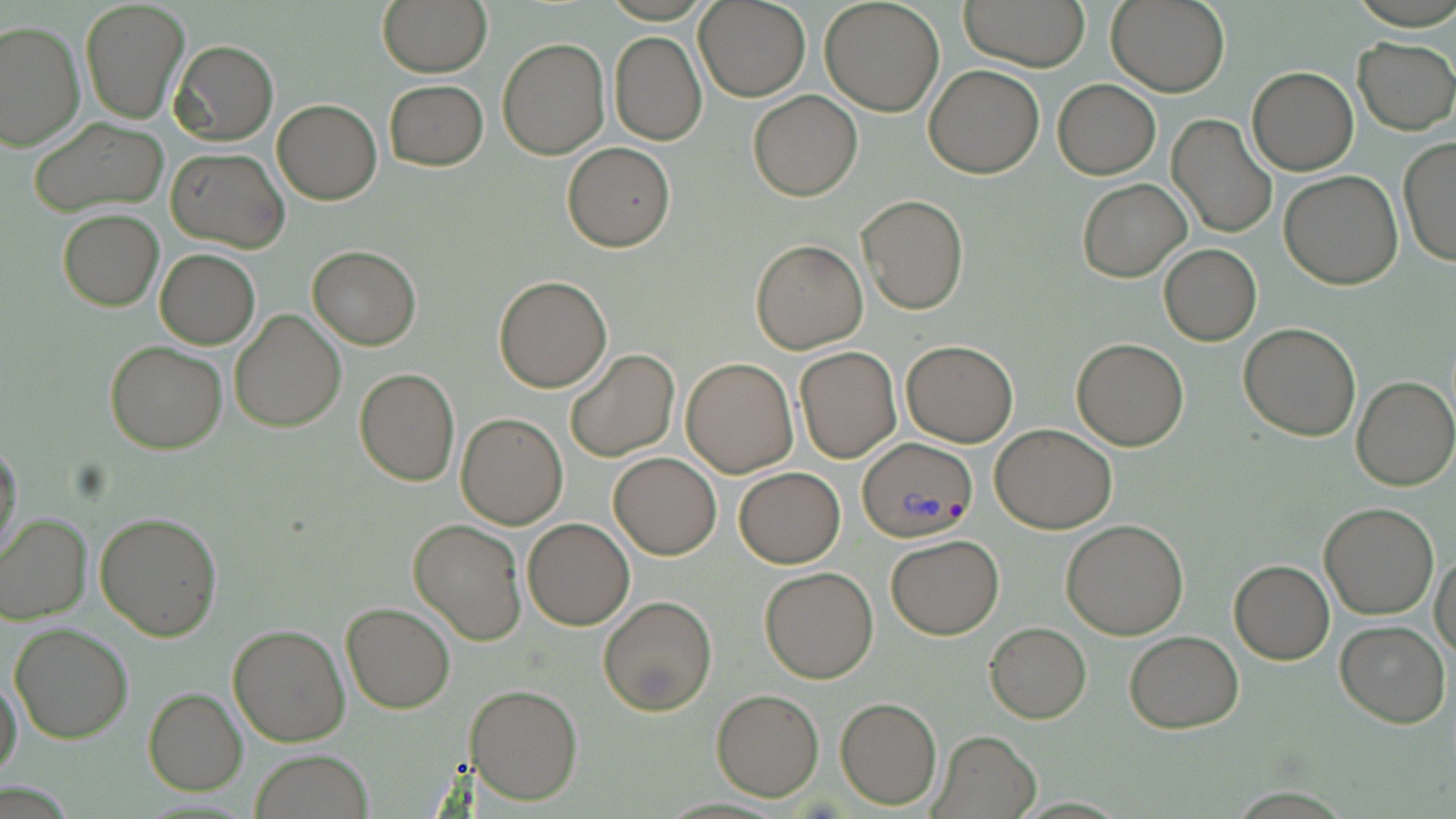
Approximate bounding boxes as [x1, y1, x2, y2] in pixels. Plasmodium vivax-infected red blood cell locations: [856, 437, 974, 543]. Uninfected red blood cell locations: [376, 0, 492, 77], [820, 0, 945, 117], [962, 0, 1091, 72], [1107, 0, 1230, 97], [80, 1, 189, 124], [694, 1, 810, 102], [0, 21, 85, 152], [609, 31, 707, 145], [497, 37, 610, 158], [1352, 37, 1456, 133], [170, 39, 278, 147], [924, 63, 1044, 179], [1247, 67, 1359, 176], [1053, 78, 1159, 179], [385, 79, 488, 170], [749, 90, 861, 202], [272, 98, 382, 205], [1167, 113, 1277, 239], [27, 117, 168, 215], [1397, 138, 1455, 265], [562, 141, 676, 251], [165, 147, 289, 253], [1279, 171, 1403, 291], [1077, 178, 1191, 283], [857, 194, 969, 316], [59, 210, 163, 311], [751, 239, 869, 354], [306, 245, 422, 349], [1159, 245, 1260, 345], [154, 249, 260, 350], [494, 275, 612, 392], [229, 309, 346, 431], [1240, 323, 1362, 440], [1071, 338, 1188, 450], [105, 341, 228, 454], [900, 341, 1018, 446], [795, 347, 900, 462], [565, 348, 679, 462], [681, 358, 798, 477], [354, 368, 460, 487], [1352, 376, 1456, 490], [457, 413, 568, 529], [989, 423, 1116, 533], [0, 439, 24, 561], [609, 453, 721, 558], [733, 467, 844, 567], [1319, 501, 1439, 619], [0, 512, 93, 624], [95, 512, 222, 641], [522, 517, 635, 630], [409, 519, 526, 645], [1061, 519, 1189, 639], [885, 535, 1002, 639], [1431, 551, 1456, 661], [1229, 560, 1334, 664], [759, 566, 879, 684], [600, 595, 717, 716], [339, 603, 455, 714], [1335, 619, 1450, 728], [985, 622, 1091, 723], [9, 623, 133, 744], [227, 623, 350, 747], [1125, 630, 1243, 733], [0, 673, 23, 783], [465, 683, 582, 805], [144, 689, 247, 796], [711, 689, 824, 801], [834, 696, 941, 809], [930, 729, 1040, 818], [250, 749, 375, 819]. Slide-level diagnosis: Plasmodium vivax. Single field of view. Thin blood film. May-Grünwald-Giemsa stain. 1000x magnification. Image is 1456×819 pixels. Light microscopy.